Comment on the morphology of the erythrocytes.
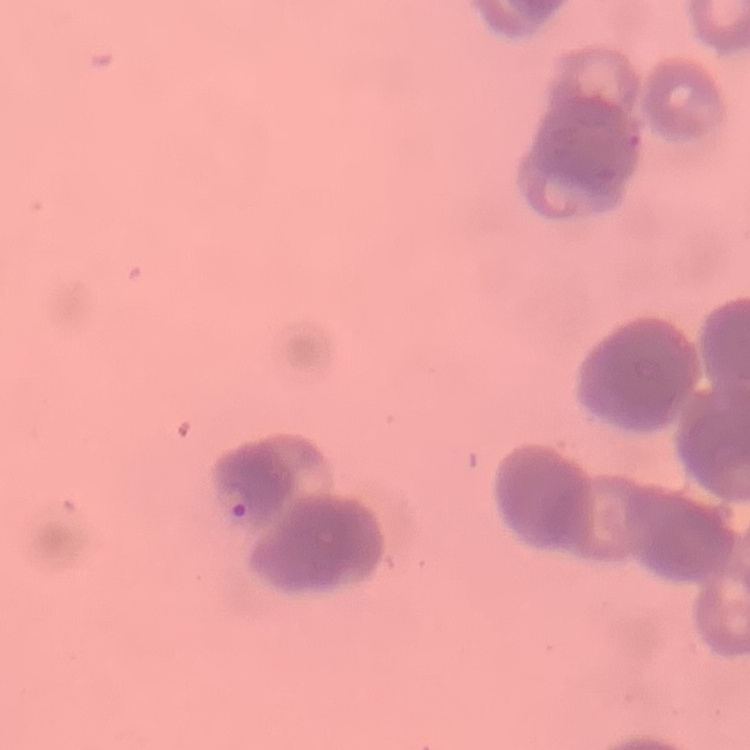

They show rouleaux formation.

Thin blood film. Stained with either Field's or Giemsa. One tile cut from a larger photomicrograph.